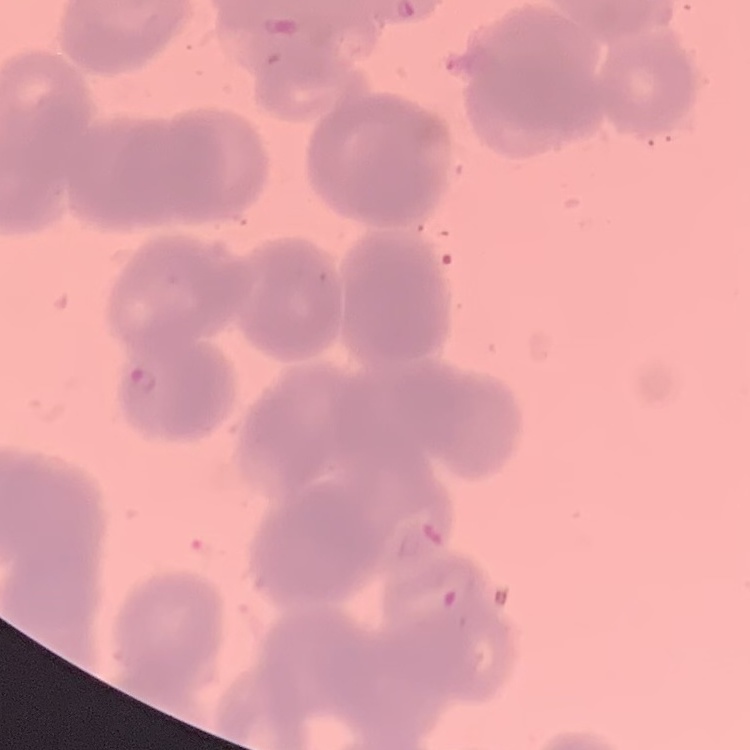

The erythrocytes exhibit rouleaux formation. Stained with either Field's or Giemsa. Thin blood film. One tile cut from a larger photomicrograph.